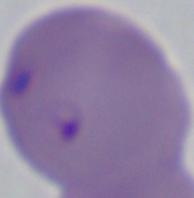
Summary:
  - Magnification: 1000x
  - Identification: Babesia
  - Modality: micrograph